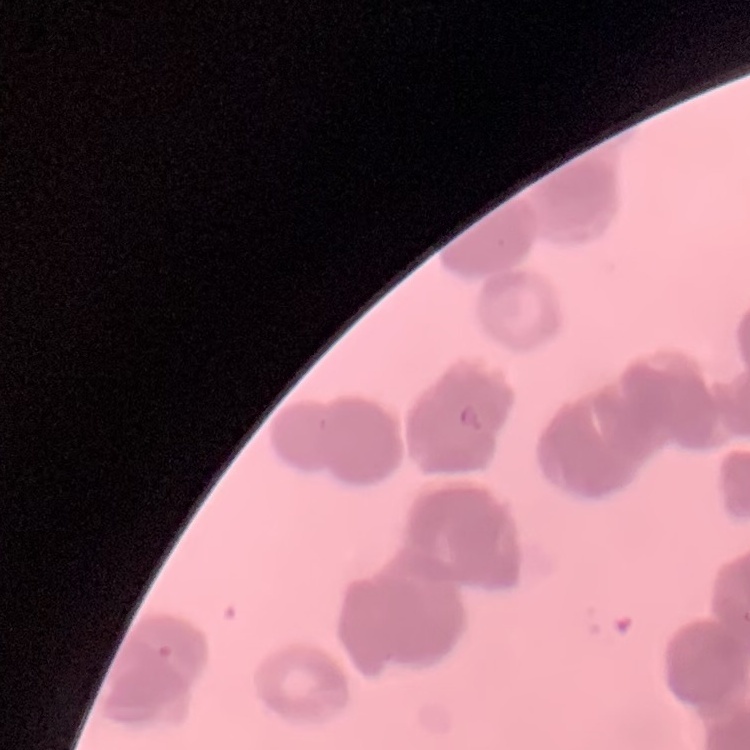

The red blood cells exhibit rouleaux formation. Thin peripheral smear. One tile cut from a larger photomicrograph. Field's or Giemsa stain.